Identify the blood parasite species.
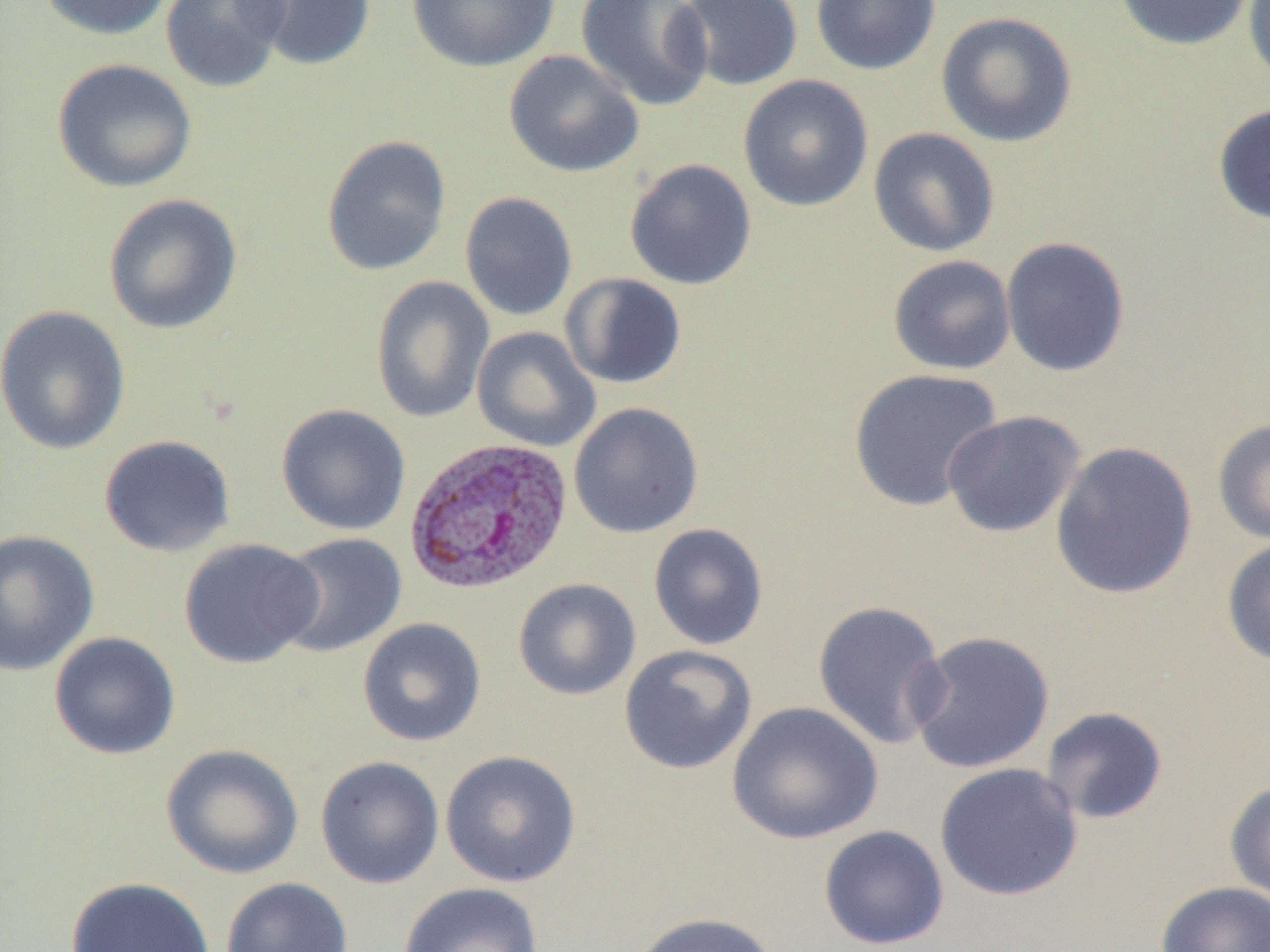
Plasmodium vivax.

Approximate bounding boxes as named x1/y1/x2/y2 corners in pixels. Plasmodium vivax-infected red blood cell locations: (x1=403, y1=436, x2=574, y2=596). Uninfected red blood cell locations: (x1=36, y1=0, x2=177, y2=40), (x1=160, y1=0, x2=290, y2=92), (x1=239, y1=0, x2=377, y2=71), (x1=406, y1=0, x2=560, y2=72), (x1=575, y1=0, x2=714, y2=111), (x1=676, y1=0, x2=803, y2=91), (x1=811, y1=0, x2=941, y2=76), (x1=1113, y1=0, x2=1255, y2=51), (x1=1242, y1=0, x2=1269, y2=90), (x1=935, y1=11, x2=1078, y2=147), (x1=503, y1=50, x2=644, y2=178), (x1=51, y1=58, x2=197, y2=193), (x1=737, y1=74, x2=874, y2=212), (x1=1212, y1=102, x2=1270, y2=225), (x1=868, y1=127, x2=1000, y2=258), (x1=320, y1=135, x2=452, y2=276), (x1=624, y1=158, x2=757, y2=290), (x1=459, y1=192, x2=578, y2=321), (x1=102, y1=193, x2=243, y2=334), (x1=1000, y1=236, x2=1130, y2=377), (x1=887, y1=254, x2=1016, y2=376), (x1=559, y1=272, x2=687, y2=390), (x1=371, y1=275, x2=495, y2=424), (x1=0, y1=304, x2=133, y2=456), (x1=471, y1=326, x2=601, y2=452), (x1=848, y1=368, x2=1004, y2=512), (x1=568, y1=402, x2=704, y2=538), (x1=276, y1=403, x2=411, y2=536), (x1=942, y1=410, x2=1086, y2=538), (x1=1212, y1=417, x2=1270, y2=544), (x1=98, y1=434, x2=235, y2=557), (x1=1049, y1=441, x2=1197, y2=599), (x1=648, y1=523, x2=769, y2=650), (x1=0, y1=529, x2=99, y2=676), (x1=275, y1=532, x2=407, y2=658), (x1=1221, y1=537, x2=1270, y2=667), (x1=178, y1=538, x2=324, y2=668), (x1=512, y1=578, x2=642, y2=700), (x1=812, y1=600, x2=950, y2=750), (x1=357, y1=617, x2=486, y2=747), (x1=906, y1=630, x2=1055, y2=774), (x1=48, y1=631, x2=181, y2=759), (x1=618, y1=644, x2=757, y2=775), (x1=726, y1=701, x2=882, y2=845), (x1=1039, y1=706, x2=1168, y2=824), (x1=160, y1=743, x2=304, y2=879), (x1=440, y1=749, x2=582, y2=887), (x1=315, y1=755, x2=445, y2=888), (x1=935, y1=762, x2=1083, y2=901), (x1=1225, y1=780, x2=1270, y2=908), (x1=818, y1=824, x2=949, y2=950), (x1=65, y1=876, x2=214, y2=952), (x1=221, y1=876, x2=353, y2=952), (x1=398, y1=881, x2=544, y2=952), (x1=1155, y1=881, x2=1270, y2=952), (x1=626, y1=912, x2=780, y2=952). 1000x magnification. Thin blood film. Single field of view. Image is 1270×952 pixels. Light microscopy.